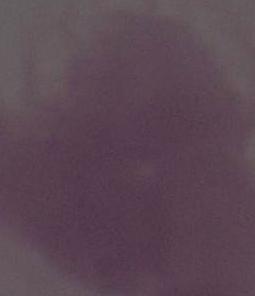

Captured at 1000x magnification. An erythrocyte is seen. Micrograph.